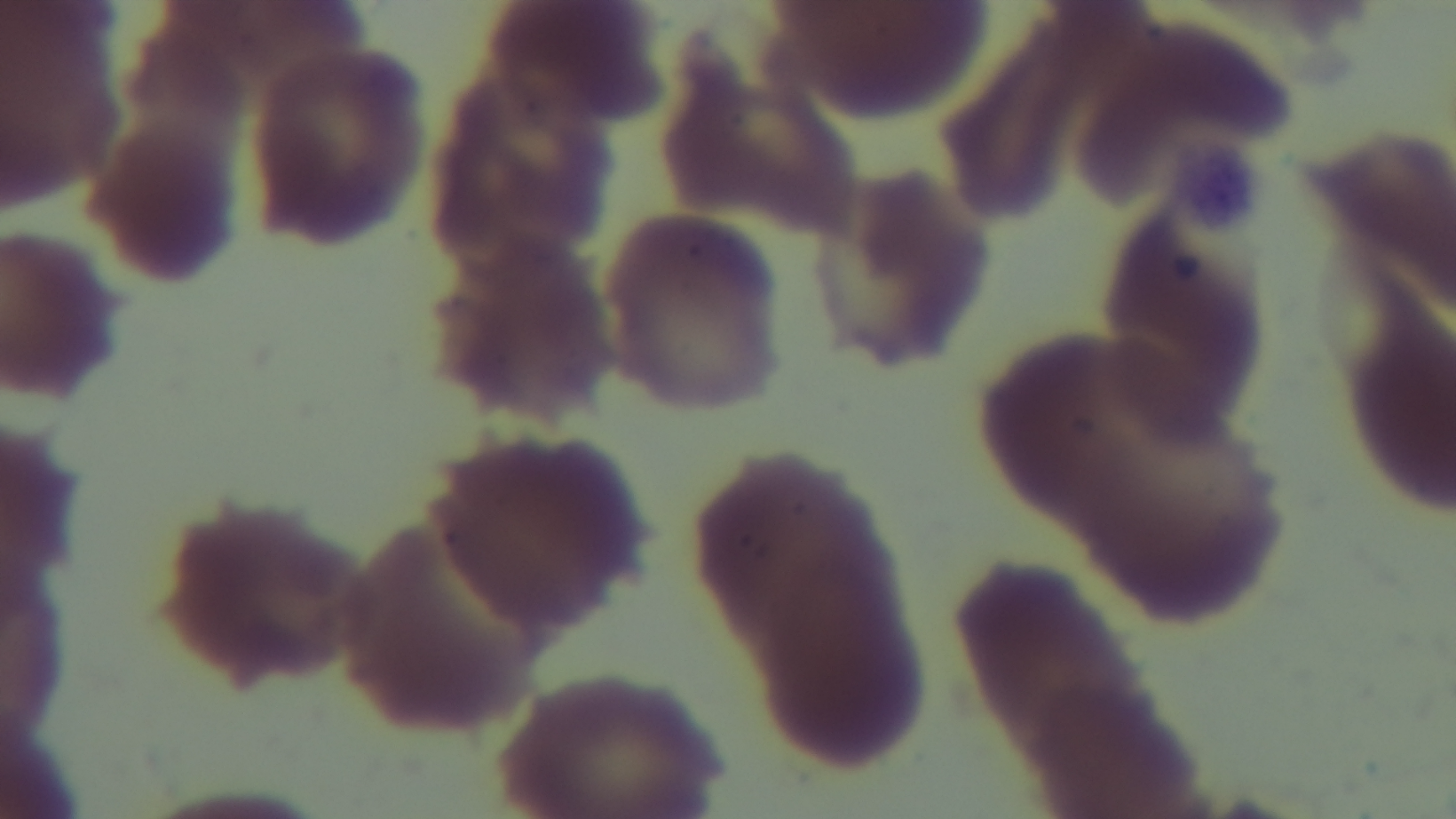
modality = light microscopy
field of view = one from the slide
capture = mounted 4K digital camera
stain = Giemsa
malaria status = negative
objective = 100x oil immersion
preparation = thin